Identify the blood parasite species.
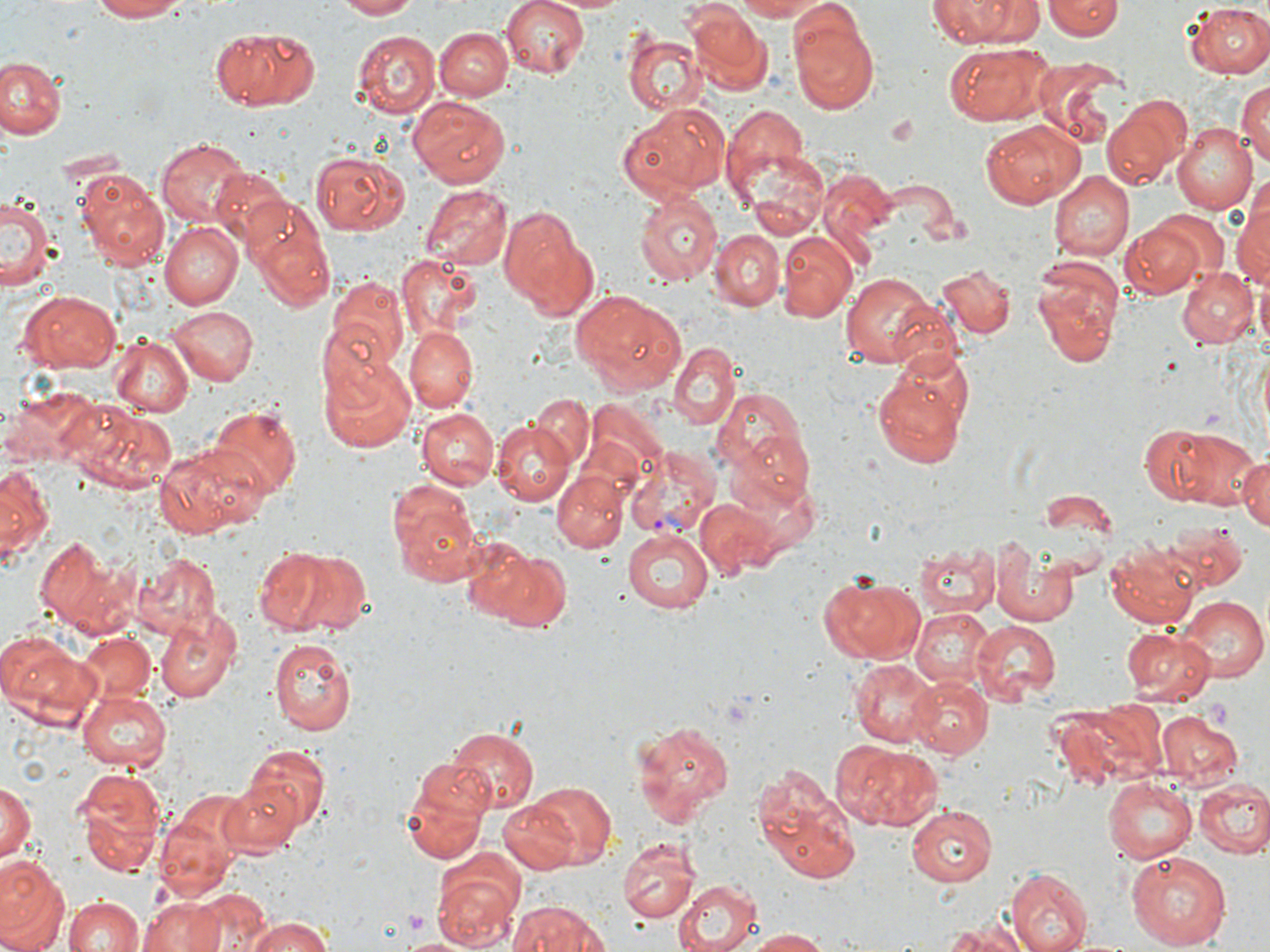
Plasmodium vivax.

platelet locations = approximate bounding boxes as [x1, y1, x2, y2] in pixels: [1205, 696, 1233, 732]
image size = 1270×952 pixels
modality = light microscopy
stain = May-Grünwald-Giemsa
preparation = thin blood smear
uninfected red blood cell locations = approximate bounding boxes as [x1, y1, x2, y2] in pixels: [89, 0, 190, 23], [334, 0, 419, 20], [500, 0, 593, 79], [550, 0, 632, 15], [733, 0, 828, 21], [930, 0, 1044, 48], [1042, 0, 1123, 41], [1185, 3, 1270, 78], [686, 8, 769, 96], [789, 11, 879, 113], [209, 25, 324, 112], [434, 28, 510, 101], [624, 28, 702, 115], [353, 29, 441, 117], [943, 44, 1054, 126], [3, 57, 66, 141], [1030, 57, 1127, 148], [1236, 77, 1270, 172], [408, 97, 512, 189], [1103, 97, 1187, 188], [619, 101, 730, 201], [722, 106, 813, 203], [979, 120, 1085, 208], [1172, 123, 1256, 214], [158, 138, 253, 229], [309, 147, 412, 234], [740, 148, 828, 238], [211, 166, 291, 246], [76, 168, 169, 267], [1048, 171, 1132, 260], [421, 185, 512, 270], [635, 192, 721, 288], [1230, 193, 1270, 298], [1, 195, 58, 293], [245, 202, 336, 313], [498, 204, 597, 316], [1119, 218, 1213, 298], [158, 220, 241, 309], [711, 231, 784, 310], [508, 233, 638, 373], [778, 233, 858, 324], [395, 254, 486, 341], [1030, 257, 1123, 370], [936, 263, 1015, 339], [1176, 265, 1256, 348], [842, 274, 945, 368], [327, 275, 408, 370], [569, 289, 687, 397], [20, 291, 121, 373], [168, 304, 257, 385], [317, 319, 396, 407], [405, 325, 478, 410], [351, 328, 481, 432], [107, 336, 193, 419], [669, 343, 741, 430], [323, 356, 417, 455], [872, 367, 970, 469], [711, 387, 806, 476], [527, 393, 594, 468], [71, 400, 179, 495], [209, 406, 300, 498], [418, 408, 497, 488], [419, 415, 571, 497], [492, 422, 574, 506], [1138, 424, 1216, 504], [1172, 428, 1265, 510], [735, 430, 816, 509], [152, 442, 269, 538], [1235, 453, 1270, 531], [1, 464, 52, 563], [552, 473, 627, 552], [390, 484, 485, 586], [1041, 489, 1115, 534], [696, 500, 776, 577], [1160, 517, 1251, 590], [620, 528, 714, 613], [34, 535, 138, 638], [460, 536, 552, 625], [1106, 539, 1203, 627], [991, 540, 1082, 625], [253, 543, 367, 637], [914, 543, 1000, 618], [490, 551, 573, 634], [133, 552, 222, 635], [818, 574, 925, 667], [1179, 597, 1266, 679], [155, 608, 243, 703], [910, 609, 995, 687], [969, 620, 1059, 703], [1119, 624, 1215, 703], [0, 633, 99, 727], [74, 634, 157, 708], [268, 638, 355, 737], [850, 659, 941, 747], [905, 677, 993, 760], [76, 688, 172, 772], [1158, 712, 1242, 788], [629, 720, 734, 829], [449, 725, 539, 814], [829, 740, 943, 832], [237, 743, 332, 839], [398, 760, 493, 864], [752, 765, 860, 886], [74, 768, 164, 877], [218, 777, 306, 856], [1103, 778, 1195, 862], [1194, 778, 1270, 859], [0, 779, 36, 867], [510, 780, 617, 871], [156, 801, 246, 904], [909, 804, 1001, 887], [617, 835, 699, 924], [1126, 851, 1233, 952], [0, 855, 69, 952], [430, 856, 523, 950], [1010, 866, 1094, 952], [673, 879, 761, 952], [189, 887, 267, 950], [63, 895, 146, 952], [137, 895, 228, 952], [507, 902, 614, 952], [239, 913, 338, 952], [931, 919, 1034, 952], [742, 929, 833, 951], [398, 935, 471, 952]
magnification = 1000x
Plasmodium vivax-infected red blood cell locations = approximate bounding boxes as [x1, y1, x2, y2] in pixels: [623, 446, 718, 538]
field of view = one of a larger specimen